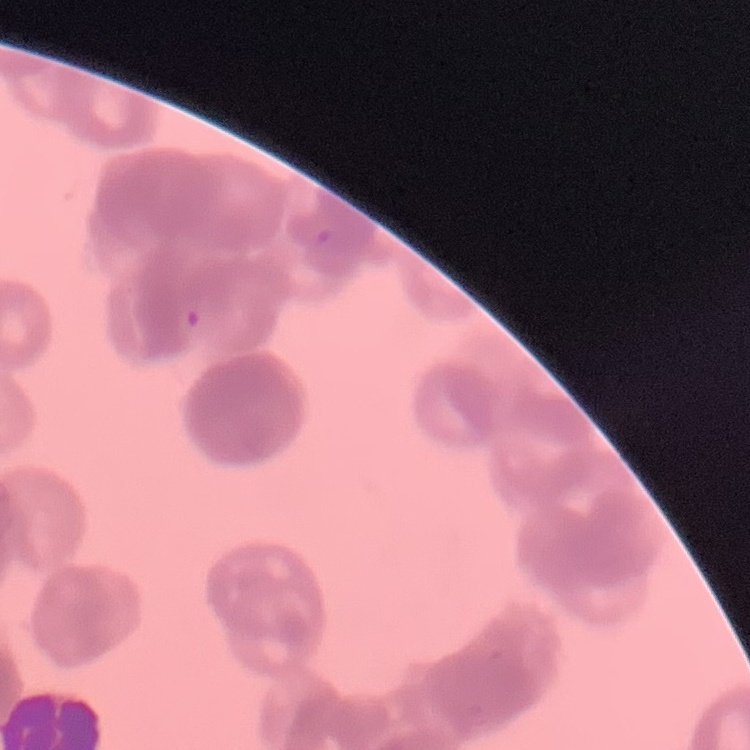

erythrocyte morphology = rouleaux formation
image type = one tile cut from a larger photomicrograph
preparation = thin blood film
stain = Field's or Giemsa